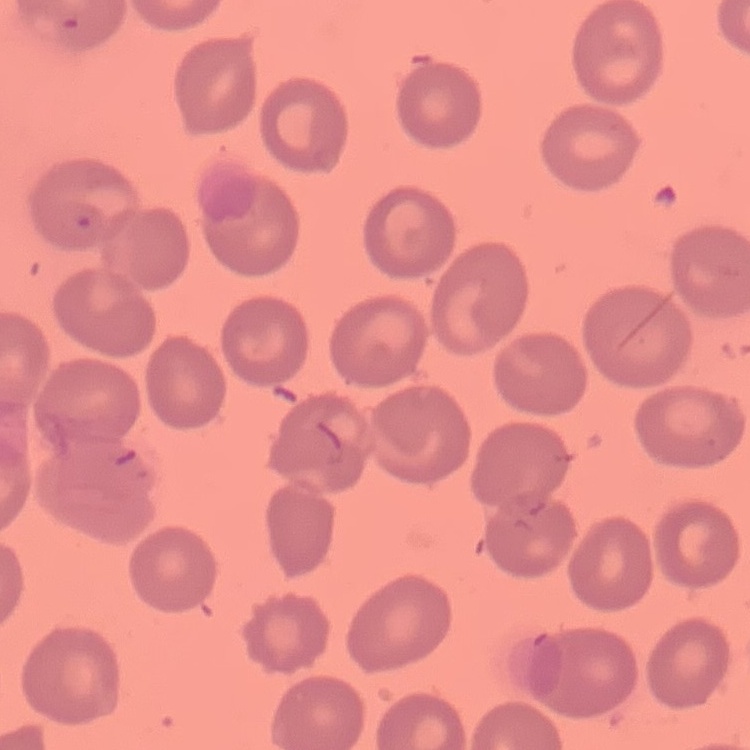
erythrocyte_morphology: no rouleaux formation
stain: Field's or Giemsa
image_type: one tile cut from a larger photomicrograph
preparation: thin blood smear